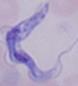
Summary:
  - Modality: micrograph
  - Identification: trypanosome
  - Magnification: 1000x